Locate every leukocyte (white blood cell).
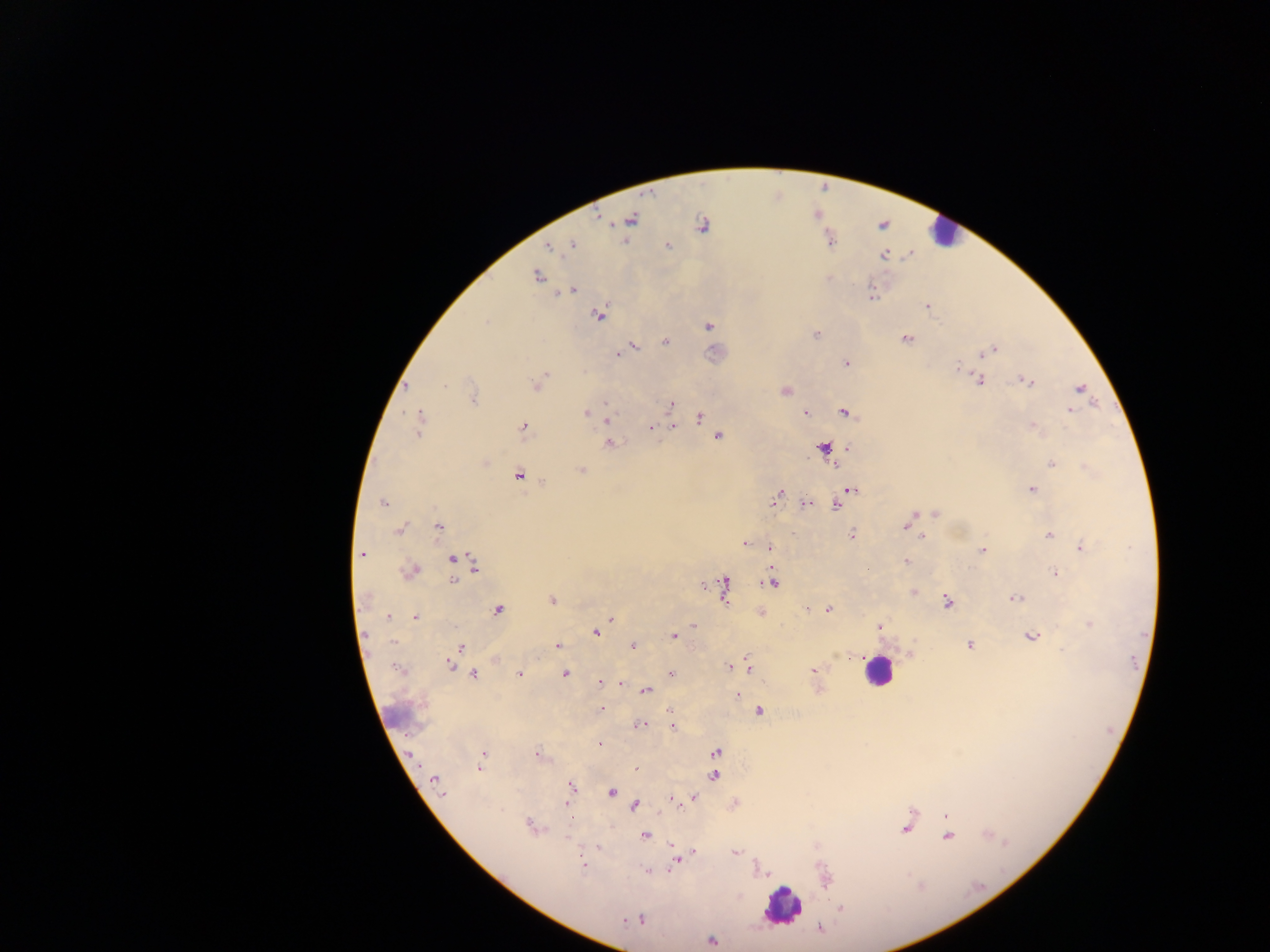
Approximate centers as (x, y) in pixels.
Leukocytes: (941, 232), (715, 352), (876, 670), (399, 715), (781, 906).

field of view = single
preparation = thick blood film
capture = mobile-phone photograph through a microscope
image size = 1270×952 pixels
country = Ghana
malaria parasite locations = approximate centers as (x, y) in pixels: (631, 219), (701, 225), (572, 245), (667, 245), (548, 247), (884, 254), (537, 276), (569, 291), (872, 298), (927, 306), (599, 315), (485, 322), (709, 326), (816, 334), (906, 339), (666, 342), (633, 346), (993, 350), (618, 354), (984, 354), (846, 364), (958, 368), (545, 376), (980, 380), (1028, 381), (536, 383), (444, 385), (1080, 389), (786, 391), (473, 398), (606, 403), (670, 406), (1070, 411), (586, 412), (806, 412), (846, 413), (700, 417), (607, 421), (420, 423), (674, 426), (522, 427), (1032, 427), (651, 428), (418, 432), (718, 436), (611, 444), (824, 448), (1052, 463), (581, 470), (519, 475), (544, 483), (851, 489), (1031, 489), (777, 498), (841, 500), (383, 503), (807, 503), (837, 505), (935, 514), (906, 525), (439, 527), (399, 529), (911, 529), (852, 534), (1049, 535), (923, 537), (745, 544), (1081, 547), (769, 548), (982, 550), (361, 554), (452, 558), (906, 561), (474, 564), (410, 571), (1054, 573), (453, 580), (772, 580), (725, 584), (704, 586), (724, 593), (914, 593), (364, 598), (1016, 598), (552, 600), (947, 602), (809, 609), (828, 609), (498, 610), (760, 614), (388, 617), (415, 617), (611, 619), (1090, 624), (693, 626), (879, 626), (596, 633), (674, 636), (1031, 636), (969, 645), (557, 646), (633, 646), (461, 647), (1062, 649), (495, 659), (448, 665), (748, 666), (728, 667), (396, 669), (814, 671), (670, 673), (519, 674), (565, 674), (474, 675), (599, 682), (621, 683), (646, 691), (737, 695), (601, 708), (759, 711), (641, 725), (673, 728), (599, 745), (484, 752), (715, 752), (536, 754), (482, 760), (637, 768), (479, 769), (714, 776), (435, 780), (571, 786), (612, 792), (442, 795), (694, 798), (672, 799), (635, 806), (946, 815), (570, 819), (529, 825), (906, 829), (646, 835), (948, 836), (673, 845), (597, 848), (693, 852), (736, 852), (676, 860), (583, 865), (647, 871), (826, 880), (841, 909), (633, 920), (640, 920), (820, 928), (712, 940)